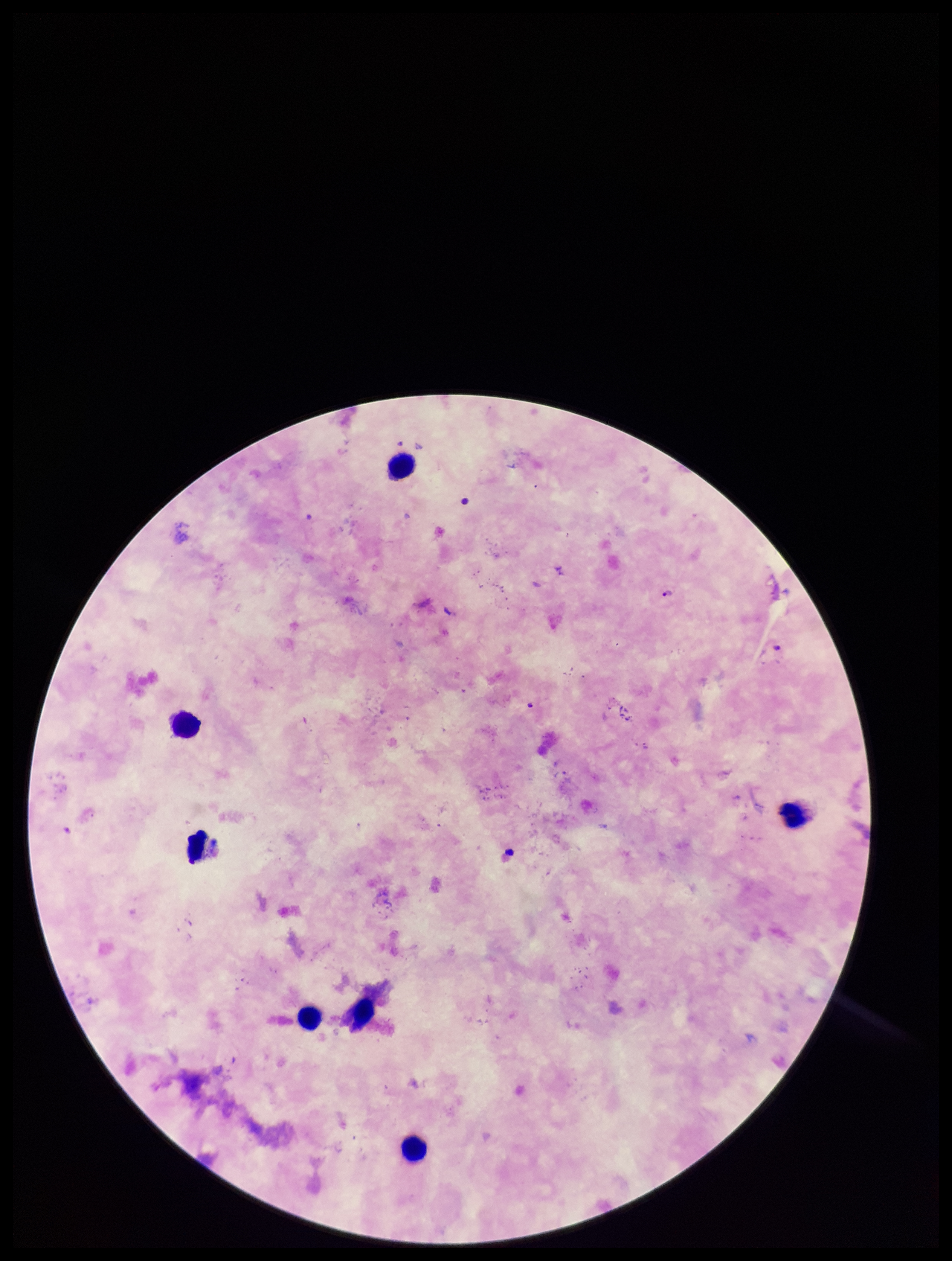

parasite count = 1
stain = Giemsa
leukocyte count = 7
capture = smartphone photograph through the microscope eyepiece
image size = 952×1261 pixels
field of view = single
species reported for this patient = Plasmodium falciparum
preparation = thick
Plasmodium parasites = detected
patient malaria status = positive